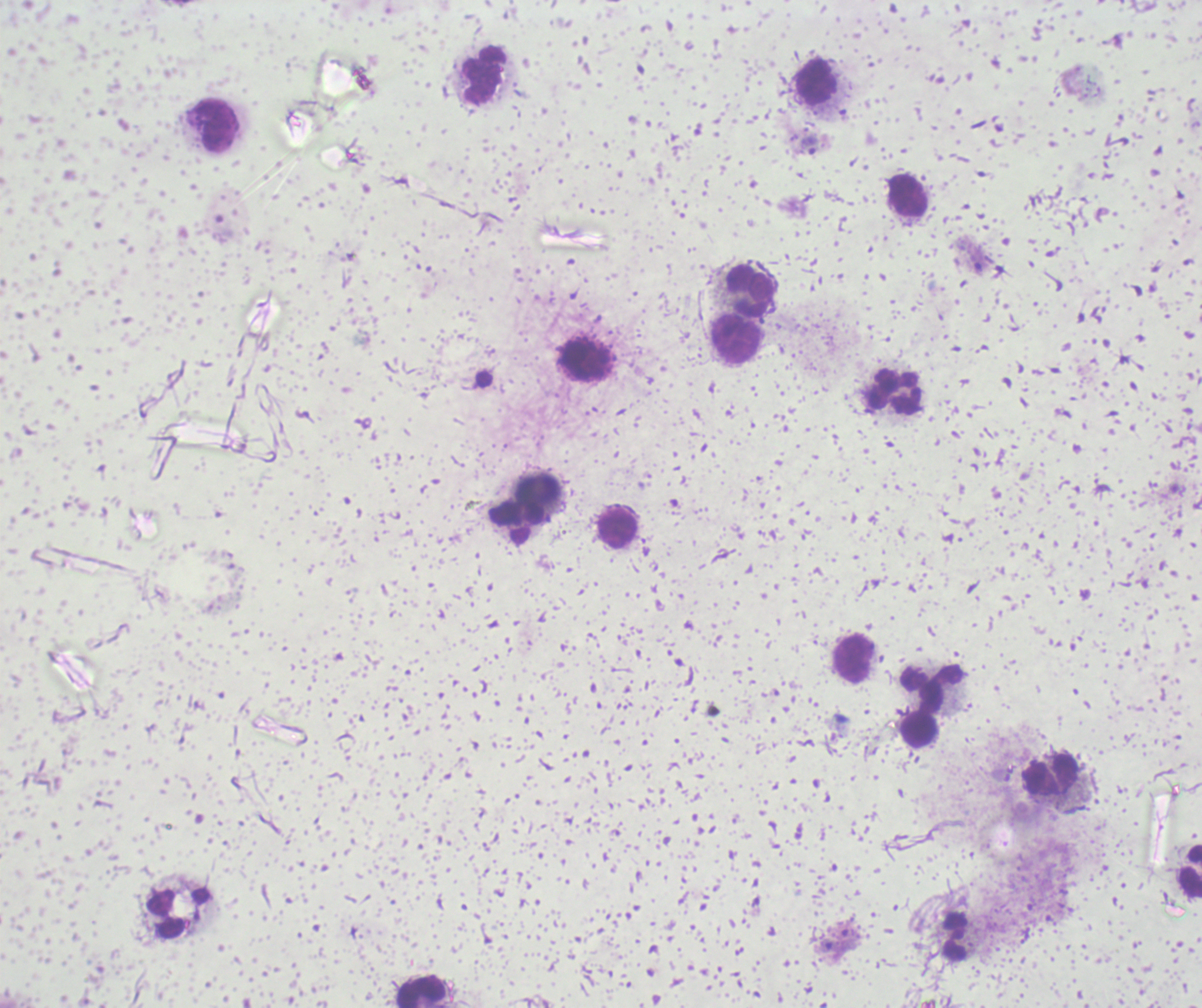
Approximate centers as {x, y} in pixels.
Summary:
  - Trophozoite locations: {808, 145}, {848, 939}, {830, 946}
  - Leukocyte locations: {483, 75}, {816, 82}, {216, 124}, {908, 196}, {749, 291}, {733, 338}, {585, 360}, {895, 393}, {537, 489}, {518, 524}, {615, 528}, {854, 659}, {932, 686}, {918, 730}, {1050, 775}, {1190, 871}, {954, 936}, {419, 991}
  - Preparation: thick blood smear
  - Result: Plasmodium parasites detected
  - Background quality: unsatisfactory
  - Field of view: one from this slide
  - Image size: 1202×1008 pixels
  - Context: previously used in an actual diagnosis
  - Magnification: 100x
  - Stain: Romanowsky